Assess this cell for malaria.
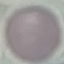

Uninfected.

Summary:
  - Capture: smartphone through the microscope eyepiece
  - Preparation: thin blood smear
  - Image type: automatically extracted cell patch, resized to 64 × 64 pixels
  - Stain: Giemsa